Mark where leukocytes are.
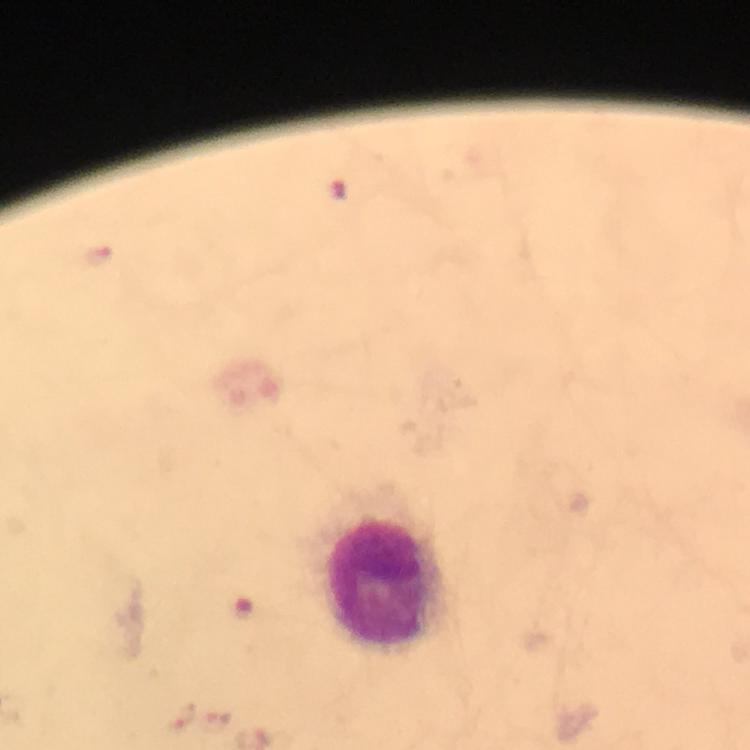
Approximate centers as [x, y] in pixels.
Leukocytes: [388, 583].

Summary:
  - Plasmodium parasite locations: [97, 257], [175, 716], [214, 722]
  - Magnification: 100x
  - Context: from a malaria diagnostic workup
  - Immersion oil: applied
  - Image size: 750×750 pixels
  - Stain: Giemsa
  - Capture: smartphone camera through the microscope
  - Cropped from: a single field of view
  - Preparation: thick blood film